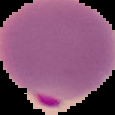
result: Plasmodium parasites detected
image_size: 115×115 pixels
image_type: segmented cell region on a black background
preparation: thin blood film